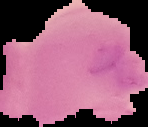
{
  "image_size": "148×127 pixels",
  "image_type": "cell region segmented out of the field of view; surrounding area masked to black",
  "preparation": "thin blood smear",
  "malaria_status": "uninfected"
}